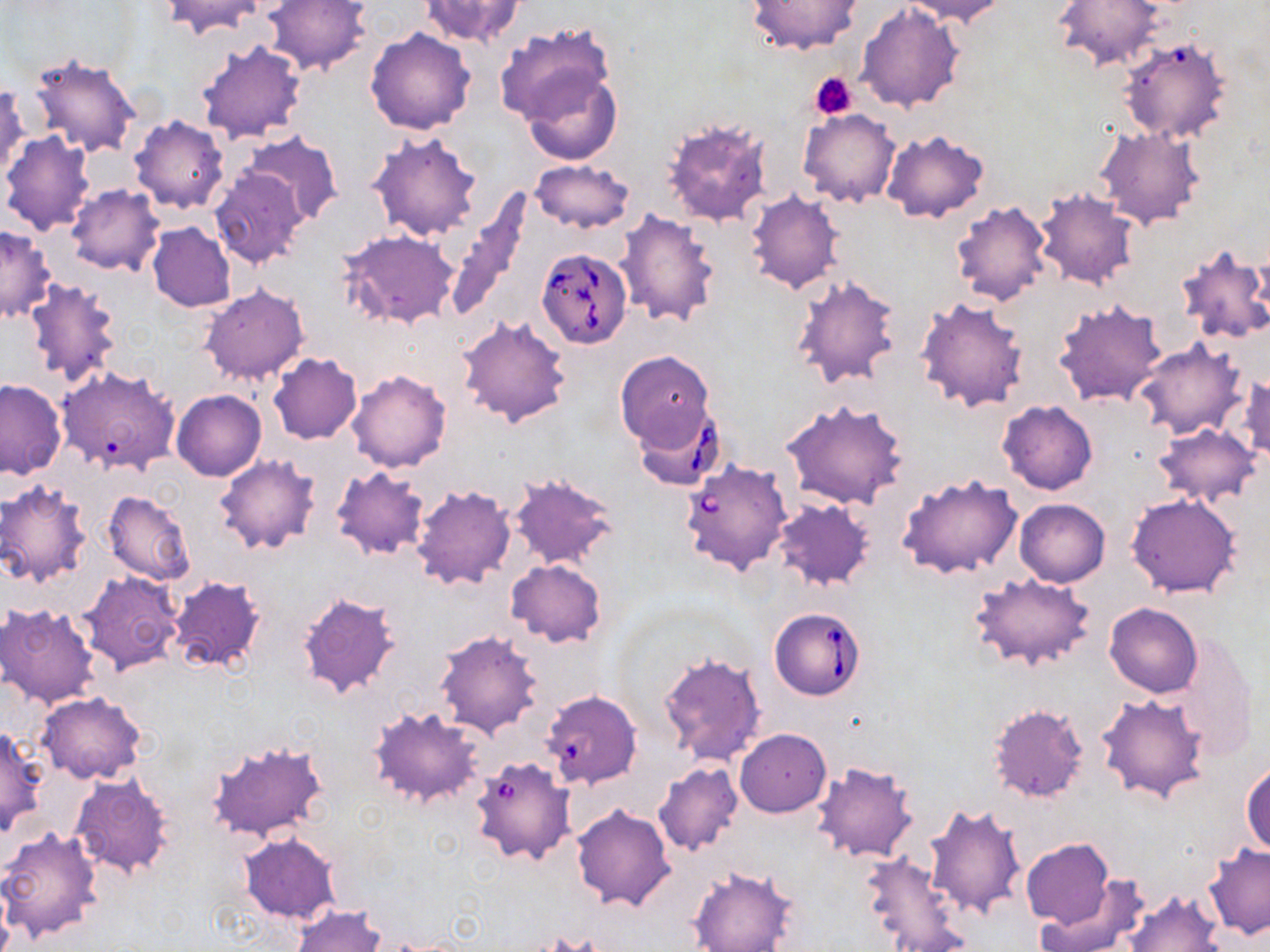
Approximate bounding boxes as (x1, y1, x2, y2) in pixels. Uninfected red blood cell locations: (160, 0, 270, 38), (418, 0, 525, 48), (744, 0, 864, 55), (902, 0, 1009, 25), (262, 1, 371, 75), (1054, 1, 1166, 72), (857, 2, 966, 111), (493, 23, 617, 134), (365, 28, 476, 136), (1117, 34, 1235, 145), (195, 38, 307, 143), (29, 52, 142, 158), (521, 68, 621, 166), (0, 84, 27, 183), (799, 108, 900, 207), (129, 115, 229, 213), (661, 116, 772, 228), (1095, 126, 1205, 230), (1, 130, 96, 236), (366, 130, 481, 241), (882, 130, 989, 223), (240, 132, 343, 226), (530, 159, 634, 234), (209, 167, 307, 270), (67, 184, 163, 275), (1035, 188, 1140, 291), (441, 190, 534, 322), (746, 190, 845, 294), (950, 201, 1052, 306), (614, 210, 721, 329), (148, 222, 236, 311), (1, 225, 57, 322), (339, 230, 460, 328), (1173, 242, 1270, 347), (790, 274, 901, 389), (22, 279, 122, 392), (200, 284, 308, 386), (916, 299, 1030, 414), (1052, 300, 1169, 409), (457, 315, 572, 428), (1135, 340, 1246, 440), (615, 352, 715, 452), (268, 353, 362, 444), (347, 369, 452, 472), (1234, 374, 1270, 463), (0, 379, 65, 479), (172, 390, 265, 481), (783, 399, 910, 510), (998, 400, 1098, 494), (1153, 422, 1260, 507), (212, 454, 321, 556), (330, 466, 429, 561), (508, 472, 618, 571), (897, 473, 1023, 581), (0, 481, 92, 589), (410, 484, 516, 591), (103, 491, 194, 585), (1126, 492, 1243, 598), (772, 497, 877, 591), (1014, 498, 1110, 587), (505, 559, 606, 647), (79, 570, 185, 675), (970, 573, 1096, 671), (168, 575, 267, 675), (296, 591, 402, 700), (1, 602, 102, 708), (1105, 602, 1202, 697), (434, 630, 544, 739), (1167, 631, 1258, 759), (660, 653, 766, 766), (36, 692, 146, 785), (1096, 693, 1211, 804), (988, 702, 1088, 804), (367, 707, 486, 810), (0, 727, 47, 836), (735, 729, 831, 817), (206, 741, 330, 843), (1242, 759, 1270, 858), (811, 761, 919, 864), (653, 762, 743, 857), (69, 773, 175, 880), (571, 803, 676, 913), (924, 803, 1027, 921), (0, 827, 104, 943), (238, 832, 343, 924), (1021, 839, 1114, 928), (1203, 844, 1269, 939), (862, 851, 968, 949), (687, 866, 796, 952), (1033, 879, 1150, 952), (1121, 888, 1223, 952), (292, 905, 384, 952). Platelet locations: (810, 70, 857, 119). Babesia divergens-infected red blood cell locations: (536, 249, 631, 348), (632, 402, 727, 491), (680, 459, 793, 576), (770, 607, 867, 700), (542, 689, 642, 789), (476, 762, 575, 864). Slide-level diagnosis: Babesia divergens. 1000x magnification. One field of a larger specimen. Thin blood smear. May-Grünwald-Giemsa stain. Light microscopy. Image is 1270×952 pixels.